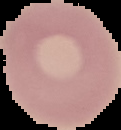 Malaria status: uninfected. Image is 121×130 pixels. Segmented cell region on a black background. From a thin blood film.